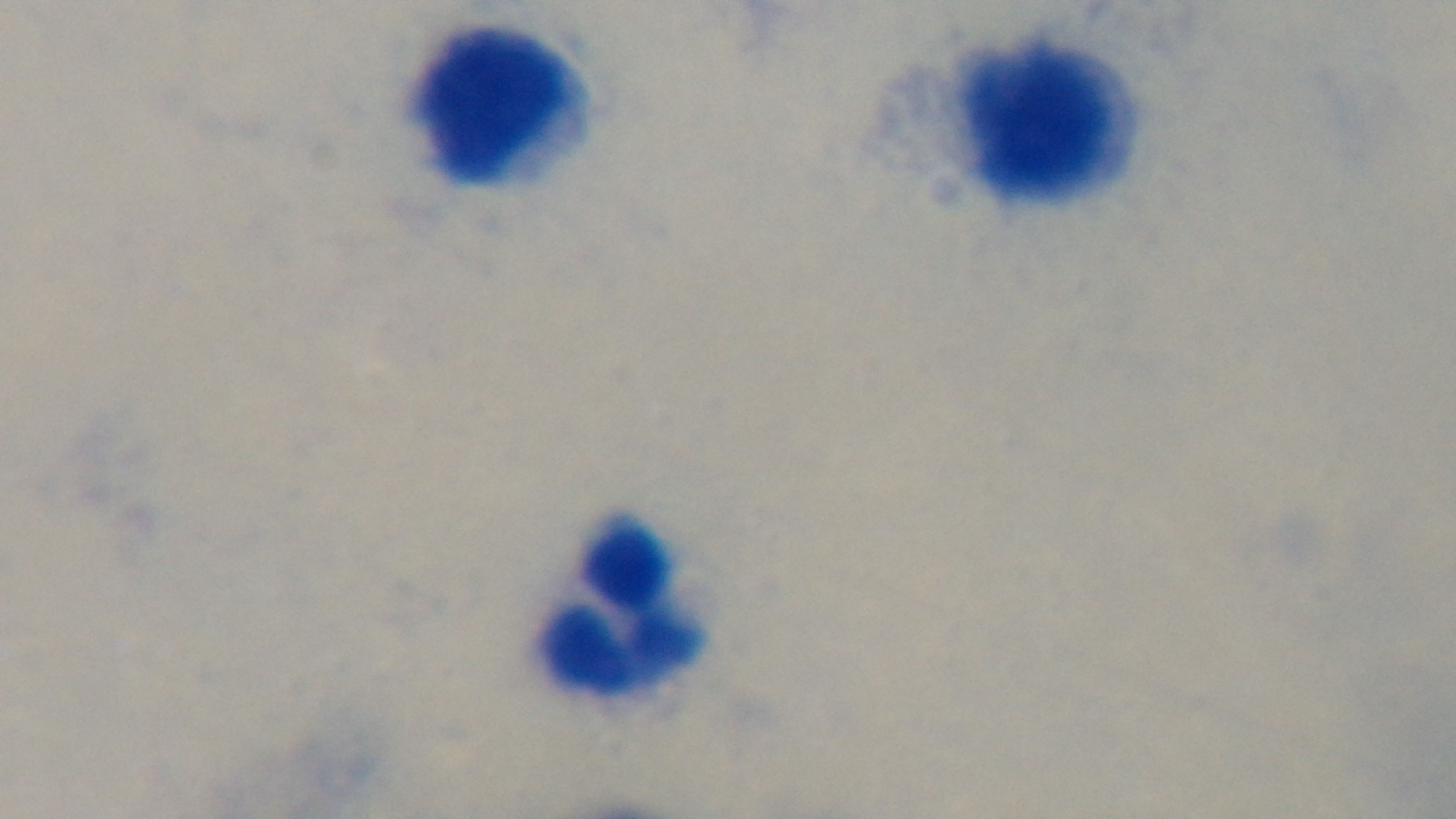
Summary:
  - Malaria status: negative
  - Objective: 100x oil immersion
  - Field of view: single
  - Capture: mounted 4K digital camera
  - Stain: Giemsa
  - Preparation: thick smear
  - Modality: light microscopy